Name the parasite shown.
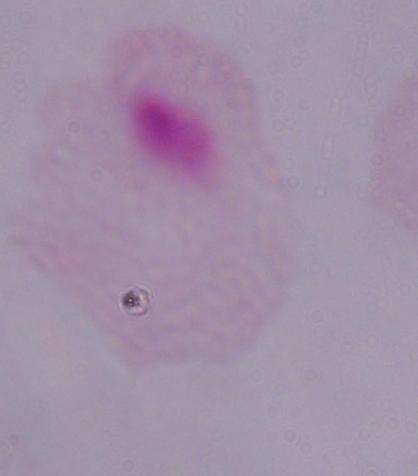

This is a trichomonad.

modality = photomicrograph
magnification = 1000x